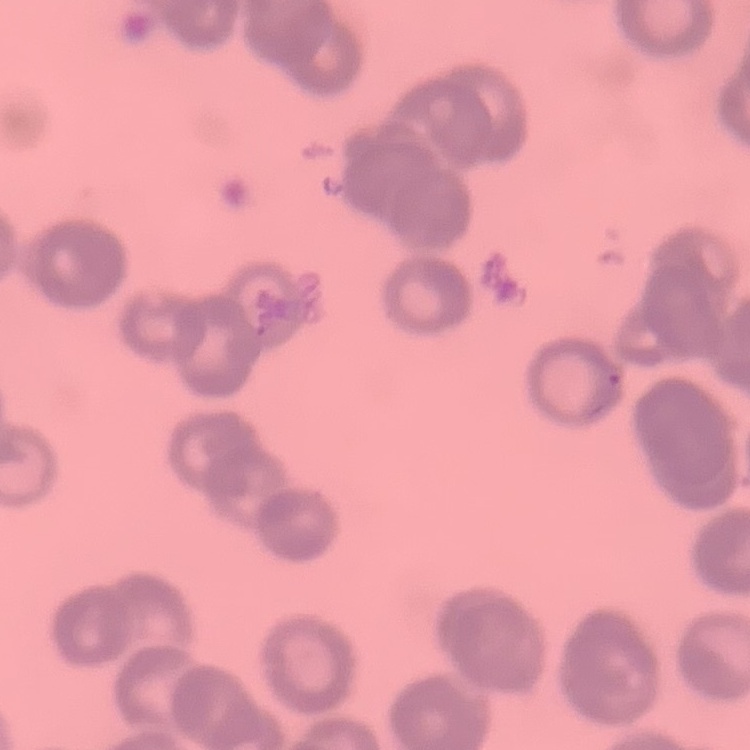

red_blood_cell_morphology: rouleaux formation
preparation: thin blood smear
stain: Field's or Giemsa
image_type: one tile cut from a larger photomicrograph